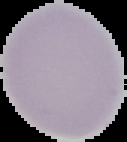 Malaria status: uninfected. From a thin blood film. Image is 127×142 pixels. The area outside the segmented cell region is set to black.